Assess the morphology of the red blood cells.
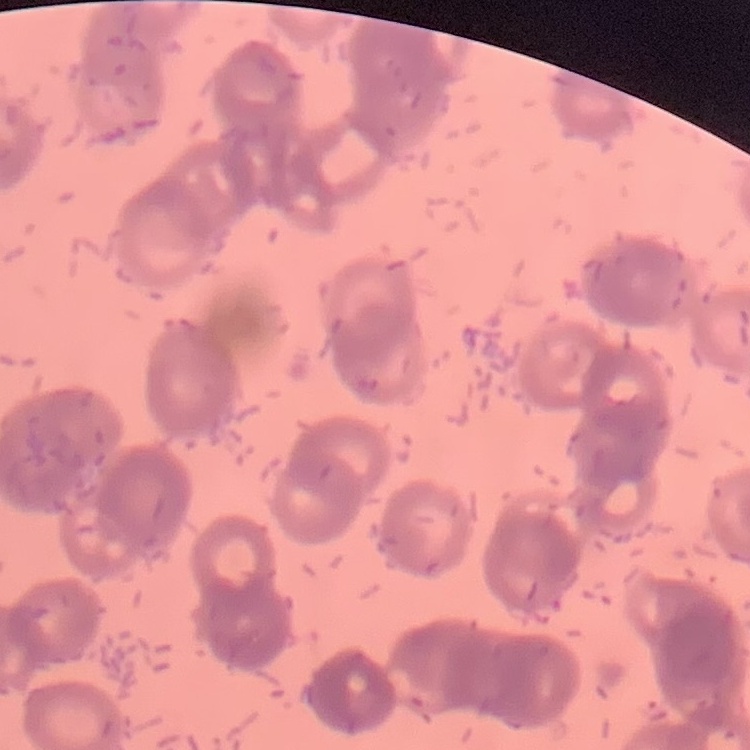

They show rouleaux formation.

preparation = thin blood smear
image type = square crop of a larger photomicrograph
stain = Field's or Giemsa